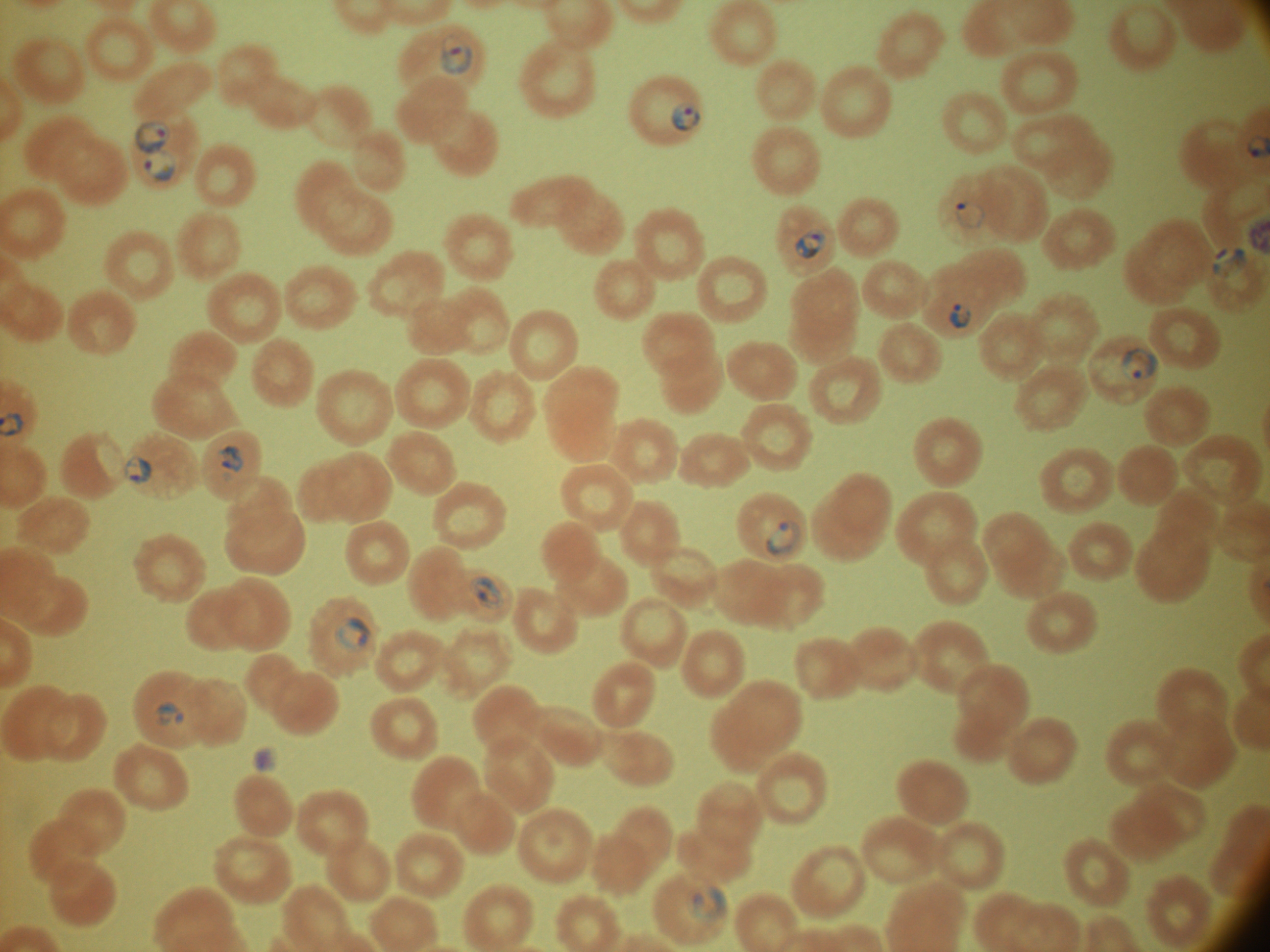

Approximate bounding boxes as (x1, y1, x2, y2) in pixels, from the source annotation, which is not necessarily exhaustive. Ring form locations: (440, 34, 473, 75), (672, 101, 701, 131), (134, 120, 171, 155), (143, 150, 177, 181), (955, 200, 986, 229), (795, 228, 828, 260), (1212, 246, 1248, 278), (949, 303, 972, 330), (1122, 347, 1159, 382), (220, 445, 244, 472), (124, 454, 152, 484), (766, 520, 802, 555), (470, 576, 504, 610), (335, 617, 371, 651), (156, 700, 185, 725), (690, 886, 728, 923). Leica DM2000 optical microscope with a built-in camera. Species: Plasmodium falciparum. 100x magnification. Single field of view. Giemsa stain. Thin blood film. Image is 1270×952 pixels.